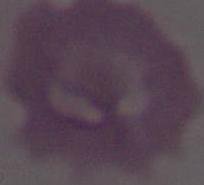

modality = photomicrograph
identification = erythrocyte
magnification = 1000x